Give the position of every Plasmodium parasite.
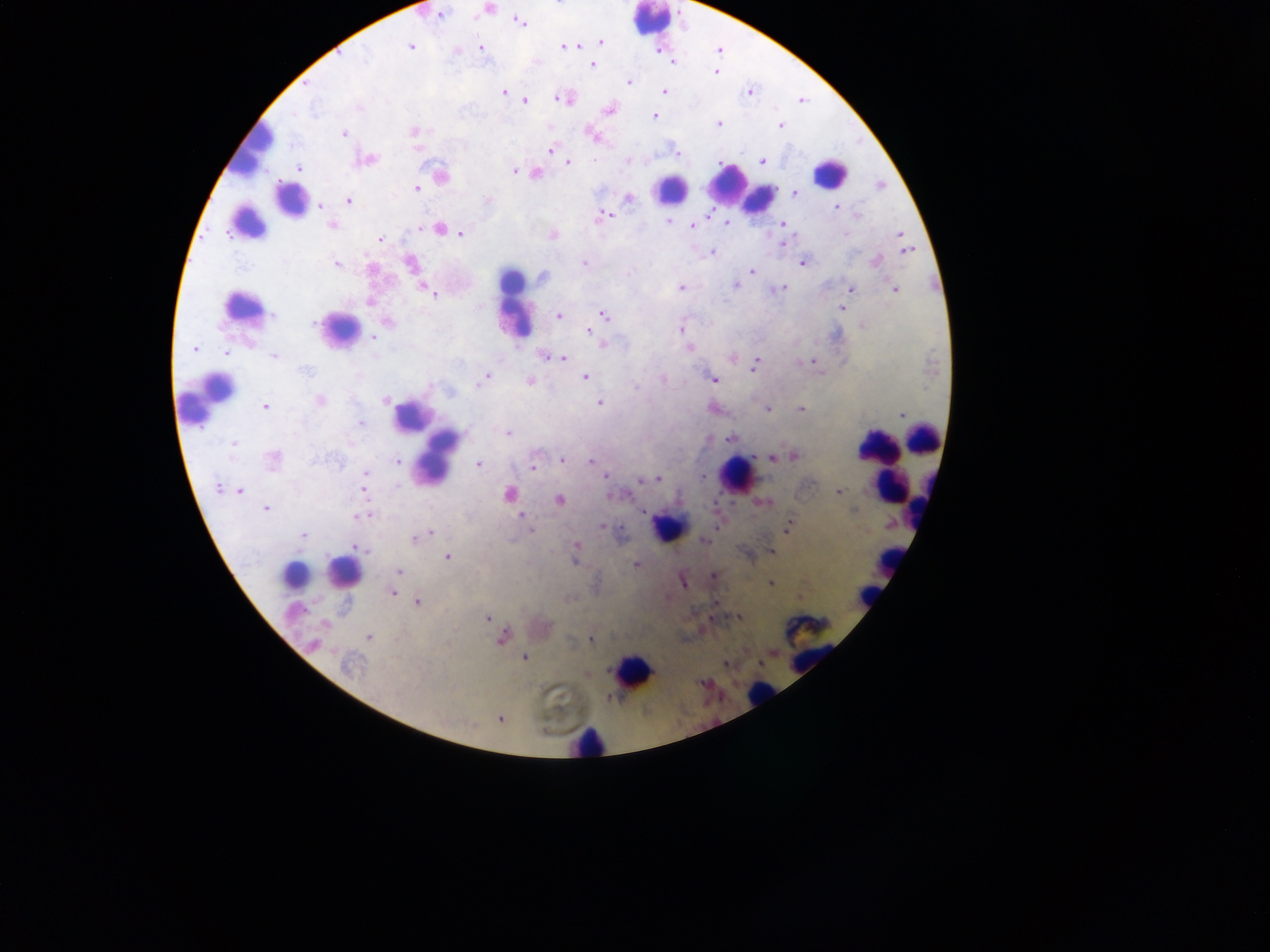

Approximate centers as [x, y] in pixels.
Plasmodium parasites: [489, 9], [440, 14], [518, 22], [601, 41], [577, 45], [411, 46], [563, 46], [479, 47], [656, 50], [719, 50], [455, 51], [672, 61], [591, 64], [716, 72], [629, 82], [503, 91], [663, 91], [749, 91], [563, 97], [801, 100], [523, 101], [609, 109], [653, 116], [718, 122], [780, 125], [414, 131], [344, 133], [594, 135], [417, 148], [551, 150], [677, 153], [365, 160], [762, 160], [567, 162], [298, 168], [513, 171], [536, 173], [441, 176], [418, 188], [795, 192], [628, 198], [347, 200], [320, 205], [836, 208], [603, 215], [857, 215], [670, 221], [726, 223], [781, 224], [331, 225], [693, 227], [418, 228], [439, 228], [460, 233], [551, 234], [899, 234], [379, 238], [783, 242], [905, 243], [712, 251], [908, 251], [875, 260], [409, 263], [802, 263], [335, 264], [583, 264], [752, 270], [541, 277], [421, 285], [733, 285], [681, 288], [782, 288], [852, 289], [893, 289], [427, 291], [431, 292], [849, 293], [368, 301], [841, 308], [602, 315], [558, 316], [386, 321], [863, 323], [590, 330], [680, 330], [373, 336], [602, 344], [688, 348], [193, 349], [226, 353], [543, 355], [274, 356], [561, 358], [732, 358], [813, 361], [754, 364], [584, 376], [487, 377], [663, 379], [713, 379], [530, 381], [319, 400], [385, 400], [600, 402], [264, 407], [712, 408], [766, 408], [800, 408], [902, 414], [360, 424], [508, 433], [730, 437], [233, 444], [792, 455], [772, 458], [273, 460], [561, 460], [399, 462], [591, 462], [478, 463], [532, 467], [365, 474], [606, 476], [702, 477], [639, 478], [657, 479], [218, 486], [362, 486], [239, 490], [838, 492], [508, 495], [610, 495], [558, 499], [763, 501], [265, 508], [643, 512], [368, 513], [362, 515], [521, 515], [602, 526], [787, 526], [530, 531], [428, 534], [303, 535], [417, 537], [706, 540], [354, 545], [576, 545], [770, 551], [447, 557], [575, 557], [635, 564], [398, 571], [712, 576], [682, 580], [771, 583], [392, 592], [799, 598], [417, 602], [738, 617], [487, 618], [501, 636], [369, 637], [591, 639], [314, 645], [524, 657], [725, 663], [349, 665], [500, 718].

Summary:
  - Leukocyte locations: [650, 20], [262, 137], [243, 160], [830, 173], [726, 183], [670, 189], [760, 199], [290, 200], [246, 222], [514, 305], [242, 307], [513, 323], [339, 329], [208, 399], [409, 416], [924, 438], [435, 459], [881, 461], [736, 474], [894, 484], [669, 527], [890, 559], [343, 573], [294, 575], [868, 595], [809, 629], [632, 671], [760, 695], [588, 742]
  - Preparation: thick blood film
  - Field of view: single
  - Capture: mobile-phone photograph through a microscope
  - Image size: 1270×952 pixels
  - Country: Ghana